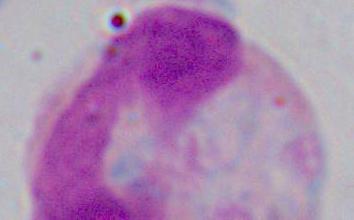
Photomicrograph. A white blood cell is shown. Captured at 1000x magnification.